Locate and identify every blood parasite.
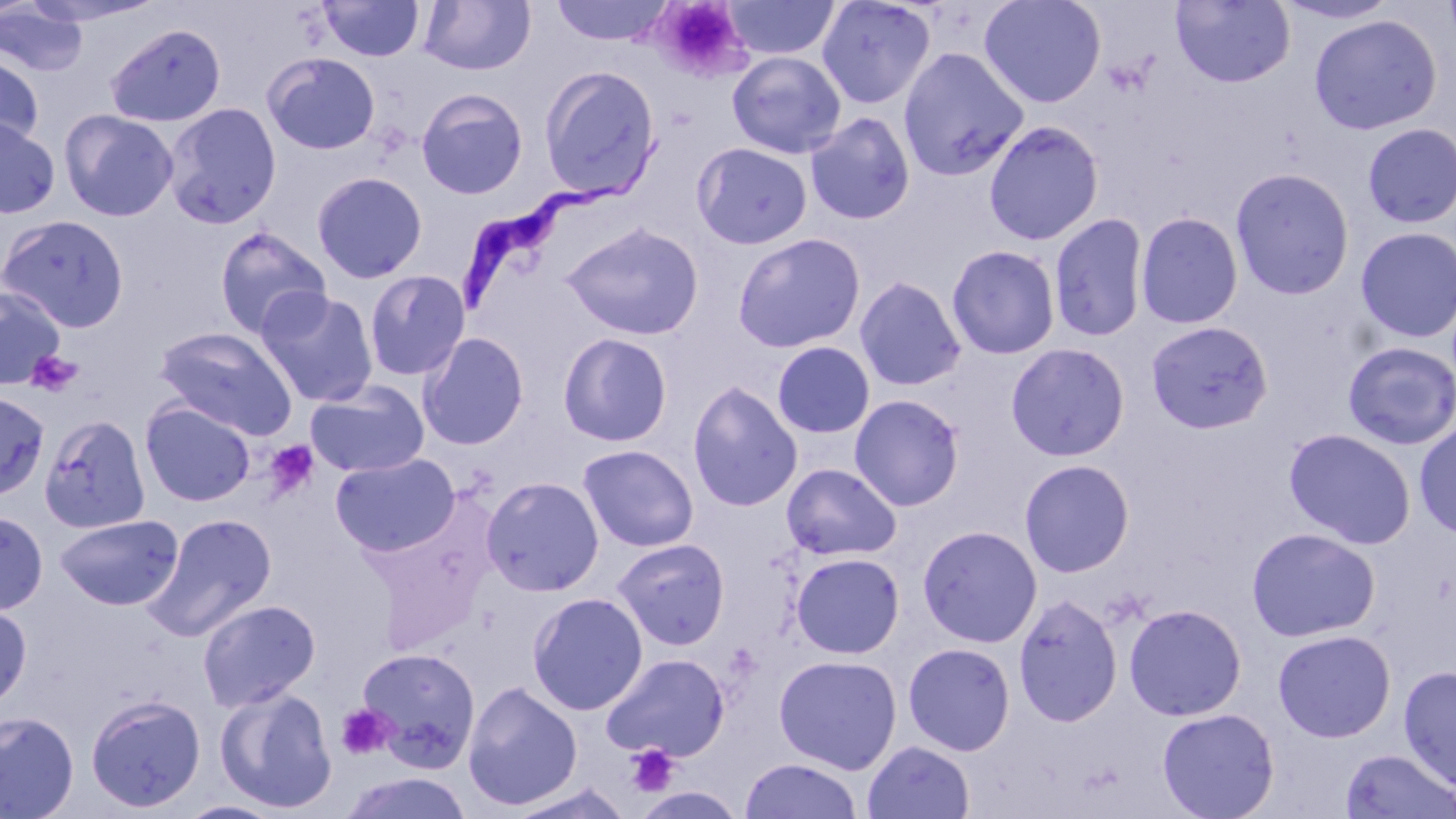
Approximate bounding boxes as (x1, y1, x2, y2) in pixels.
Trypanosoma brucei: (454, 127, 677, 309).
No Plasmodium falciparum, Plasmodium ovale, Plasmodium malariae, Plasmodium vivax, or Babesia divergens observed.

slide-level diagnosis = Trypanosoma brucei
modality = optical microscopy
platelet locations = approximate bounding boxes as (x1, y1, x2, y2) in pixels: (652, 2, 750, 77), (25, 350, 82, 396), (263, 440, 321, 501), (335, 704, 395, 760), (626, 745, 681, 797)
image size = 1456×819 pixels
uninfected red blood cell locations = approximate bounding boxes as (x1, y1, x2, y2) in pixels: (318, 0, 425, 61), (418, 0, 536, 76), (550, 0, 673, 46), (722, 0, 840, 61), (815, 0, 936, 109), (978, 0, 1107, 109), (1170, 0, 1296, 88), (1275, 0, 1400, 26), (0, 3, 89, 77), (1309, 14, 1442, 135), (105, 23, 226, 128), (898, 47, 1029, 181), (263, 51, 381, 155), (727, 51, 846, 159), (0, 53, 43, 152), (539, 65, 662, 201), (416, 88, 529, 200), (162, 102, 282, 229), (59, 108, 179, 222), (805, 112, 916, 225), (0, 116, 60, 219), (983, 120, 1104, 246), (1362, 122, 1456, 229), (692, 142, 813, 250), (1229, 167, 1355, 300), (311, 171, 428, 284), (1134, 211, 1244, 329), (1048, 212, 1150, 342), (0, 215, 130, 332), (560, 222, 705, 341), (213, 225, 332, 340), (1354, 226, 1456, 344), (732, 233, 866, 353), (946, 244, 1061, 359), (363, 270, 470, 381), (854, 276, 967, 391), (0, 286, 66, 389), (256, 288, 379, 408), (1146, 320, 1273, 434), (154, 326, 299, 439), (417, 332, 529, 451), (557, 332, 672, 447), (1342, 341, 1456, 450), (773, 342, 875, 439), (1006, 343, 1130, 462), (305, 380, 430, 478), (687, 381, 803, 512), (0, 390, 51, 501), (849, 394, 965, 511), (140, 400, 256, 507), (40, 413, 150, 535), (1414, 420, 1456, 540), (1282, 427, 1417, 549), (577, 444, 700, 552), (330, 452, 460, 557), (1019, 459, 1135, 578), (781, 462, 902, 561), (480, 476, 604, 597), (0, 509, 48, 615), (143, 513, 277, 641), (55, 514, 183, 610), (917, 525, 1042, 648), (1246, 527, 1381, 643), (612, 539, 730, 651), (790, 552, 905, 658), (527, 592, 649, 715), (1013, 594, 1123, 728), (197, 598, 320, 712), (0, 602, 32, 710), (1123, 603, 1247, 721), (1273, 629, 1395, 742), (903, 642, 1016, 756), (355, 647, 481, 771), (602, 653, 729, 761), (773, 655, 902, 775), (1398, 665, 1456, 793), (463, 681, 583, 811), (214, 685, 338, 814), (85, 693, 206, 813), (1157, 708, 1280, 819), (0, 711, 79, 819), (862, 740, 975, 819), (1339, 747, 1456, 819), (740, 757, 863, 818), (340, 771, 473, 818), (508, 783, 634, 819), (175, 801, 286, 819)
field of view = one of a larger specimen
magnification = 1000x
stain = May-Grünwald-Giemsa
preparation = thin blood film